Give the extent of all Babesia divergens-infected red blood cells.
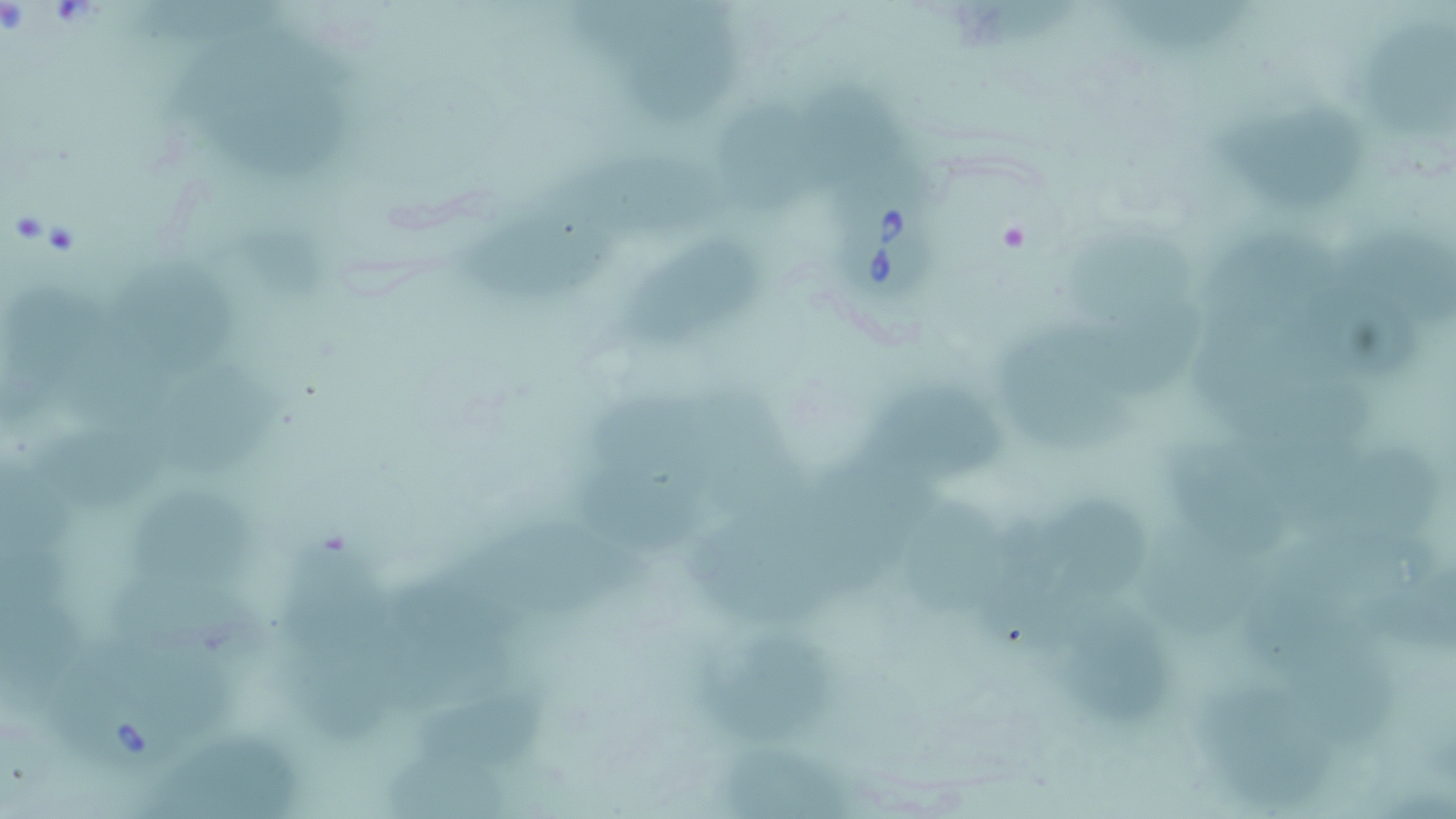

Approximate bounding boxes as named x1/y1/x2/y2 corners in pixels.
Babesia divergens-infected red blood cells: (x1=843, y1=180, x2=941, y2=301).

Uninfected red blood cell locations: (x1=1119, y1=2, x2=1259, y2=60), (x1=629, y1=10, x2=745, y2=127), (x1=1361, y1=17, x2=1455, y2=145), (x1=174, y1=30, x2=370, y2=115), (x1=192, y1=85, x2=351, y2=188), (x1=816, y1=85, x2=922, y2=188), (x1=711, y1=89, x2=835, y2=223), (x1=1213, y1=100, x2=1377, y2=216), (x1=560, y1=152, x2=732, y2=246), (x1=468, y1=208, x2=622, y2=309), (x1=1329, y1=214, x2=1452, y2=330), (x1=1063, y1=216, x2=1200, y2=330), (x1=1208, y1=224, x2=1349, y2=355), (x1=635, y1=232, x2=764, y2=353), (x1=100, y1=255, x2=247, y2=387), (x1=11, y1=282, x2=133, y2=391), (x1=1085, y1=303, x2=1199, y2=401), (x1=1001, y1=324, x2=1131, y2=452), (x1=1205, y1=346, x2=1375, y2=447), (x1=155, y1=365, x2=287, y2=473), (x1=859, y1=383, x2=1012, y2=481), (x1=701, y1=384, x2=815, y2=530), (x1=597, y1=388, x2=724, y2=503), (x1=42, y1=428, x2=174, y2=522), (x1=1169, y1=442, x2=1296, y2=562), (x1=1311, y1=447, x2=1439, y2=548), (x1=810, y1=452, x2=948, y2=548), (x1=580, y1=471, x2=729, y2=557), (x1=125, y1=480, x2=263, y2=596), (x1=912, y1=495, x2=1016, y2=619), (x1=1048, y1=499, x2=1156, y2=621), (x1=991, y1=506, x2=1083, y2=651), (x1=458, y1=507, x2=656, y2=625), (x1=701, y1=518, x2=842, y2=628), (x1=1133, y1=523, x2=1263, y2=639), (x1=284, y1=541, x2=405, y2=666), (x1=1377, y1=557, x2=1456, y2=651), (x1=1245, y1=566, x2=1370, y2=686), (x1=377, y1=572, x2=525, y2=700), (x1=106, y1=573, x2=287, y2=676), (x1=0, y1=581, x2=111, y2=715), (x1=1068, y1=608, x2=1184, y2=733), (x1=1295, y1=632, x2=1406, y2=746), (x1=715, y1=640, x2=838, y2=741), (x1=54, y1=645, x2=205, y2=772), (x1=287, y1=653, x2=405, y2=745), (x1=1207, y1=680, x2=1329, y2=817), (x1=418, y1=692, x2=546, y2=782), (x1=157, y1=727, x2=300, y2=819), (x1=725, y1=739, x2=858, y2=819). Slide-level diagnosis: Babesia divergens. Thin blood smear. Image is 1456×819 pixels. One field of a larger specimen. 1000x magnification. Optical microscopy. May-Grünwald-Giemsa-stained preparation.